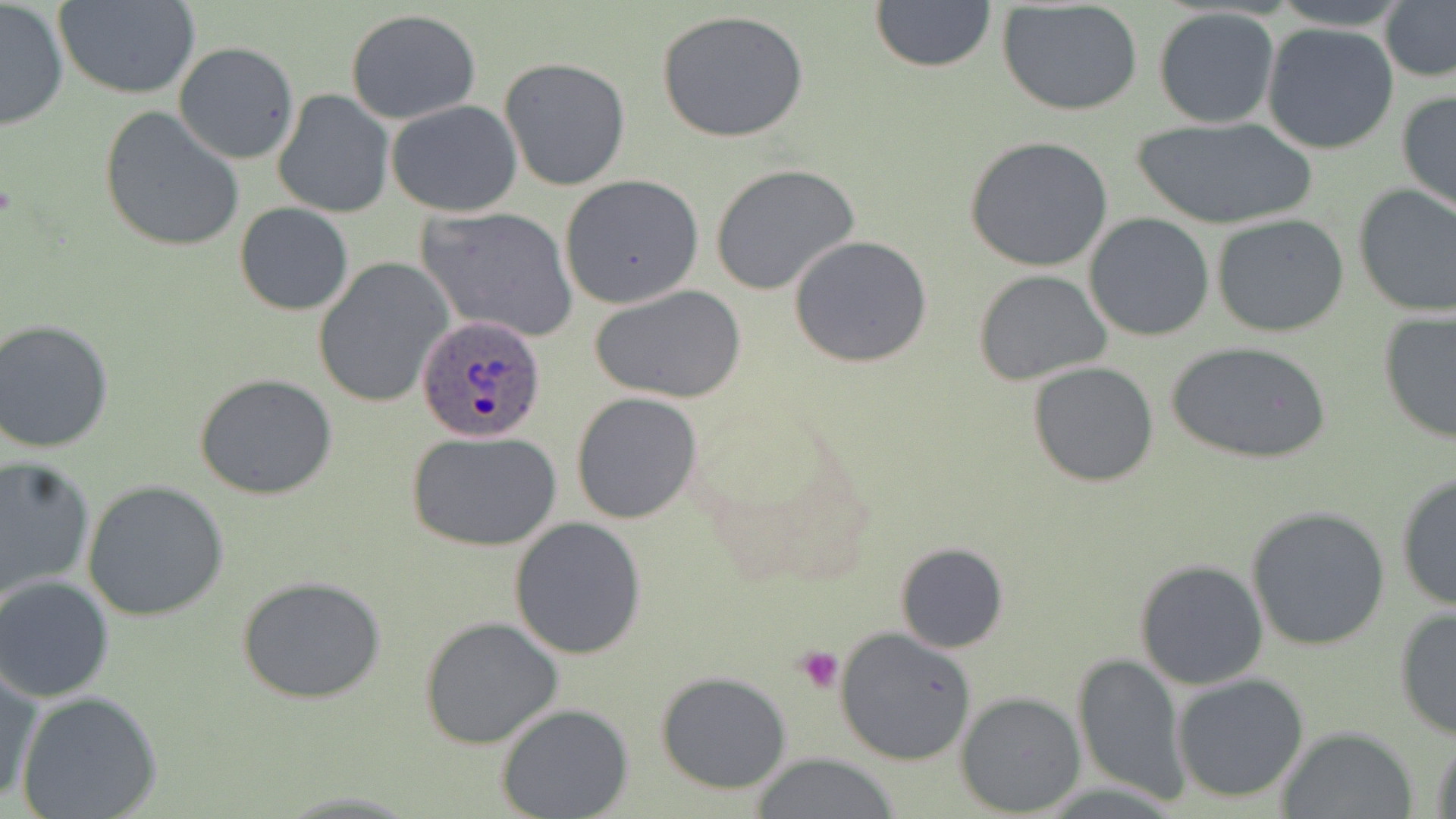

{
  "slide_level_diagnosis": "Plasmodium ovale",
  "magnification": "1000x",
  "stain": "May-Grünwald-Giemsa",
  "platelet_locations": "approximate bounding boxes as [x1, y1, x2, y2] in pixels: [795, 646, 845, 694]",
  "preparation": "thin blood smear",
  "image_size": "1456×819 pixels",
  "plasmodium_ovale_infected_red_blood_cell_locations": "approximate bounding boxes as [x1, y1, x2, y2] in pixels: [416, 315, 549, 443]",
  "field_of_view": "one of a larger specimen",
  "uninfected_red_blood_cell_locations": "approximate bounding boxes as [x1, y1, x2, y2] in pixels: [56, 0, 202, 100], [1268, 0, 1410, 31], [1379, 0, 1456, 85], [0, 1, 69, 131], [870, 1, 997, 74], [996, 2, 1144, 118], [657, 8, 811, 144], [1153, 8, 1280, 129], [346, 9, 480, 125], [1261, 22, 1401, 155], [174, 41, 299, 164], [500, 57, 630, 191], [1396, 89, 1456, 216], [273, 90, 394, 218], [392, 90, 540, 321], [386, 100, 522, 217], [98, 107, 245, 254], [1132, 116, 1318, 231], [963, 136, 1115, 273], [710, 163, 861, 295], [559, 175, 703, 308], [1352, 183, 1456, 317], [235, 201, 353, 316], [416, 206, 579, 343], [1084, 213, 1215, 342], [1211, 214, 1350, 338], [789, 235, 933, 368], [314, 257, 453, 409], [972, 269, 1112, 385], [589, 283, 747, 405], [1377, 309, 1456, 444], [1, 318, 118, 454], [1166, 342, 1330, 466], [1027, 362, 1160, 487], [195, 373, 337, 499], [572, 392, 702, 524], [409, 431, 560, 552], [0, 455, 95, 600], [1394, 473, 1456, 612], [81, 479, 230, 622], [1245, 505, 1392, 651], [508, 517, 647, 658], [894, 541, 1009, 653], [1133, 558, 1268, 689], [0, 575, 118, 703], [237, 576, 387, 705], [1393, 608, 1456, 741], [419, 616, 564, 749], [835, 626, 978, 765], [1072, 652, 1189, 807], [0, 668, 43, 809], [654, 670, 792, 793], [1171, 671, 1309, 804], [15, 691, 163, 819], [956, 691, 1086, 816], [497, 705, 633, 819], [1428, 727, 1456, 819], [1274, 728, 1419, 818], [749, 754, 906, 819]",
  "modality": "optical microscopy"
}